Assess this cell for malaria.
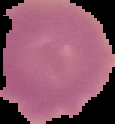

It is uninfected.

{
  "image_type": "cell region segmented out of the field of view; surrounding area masked to black",
  "image_size": "115×124 pixels",
  "preparation": "thin blood smear"
}